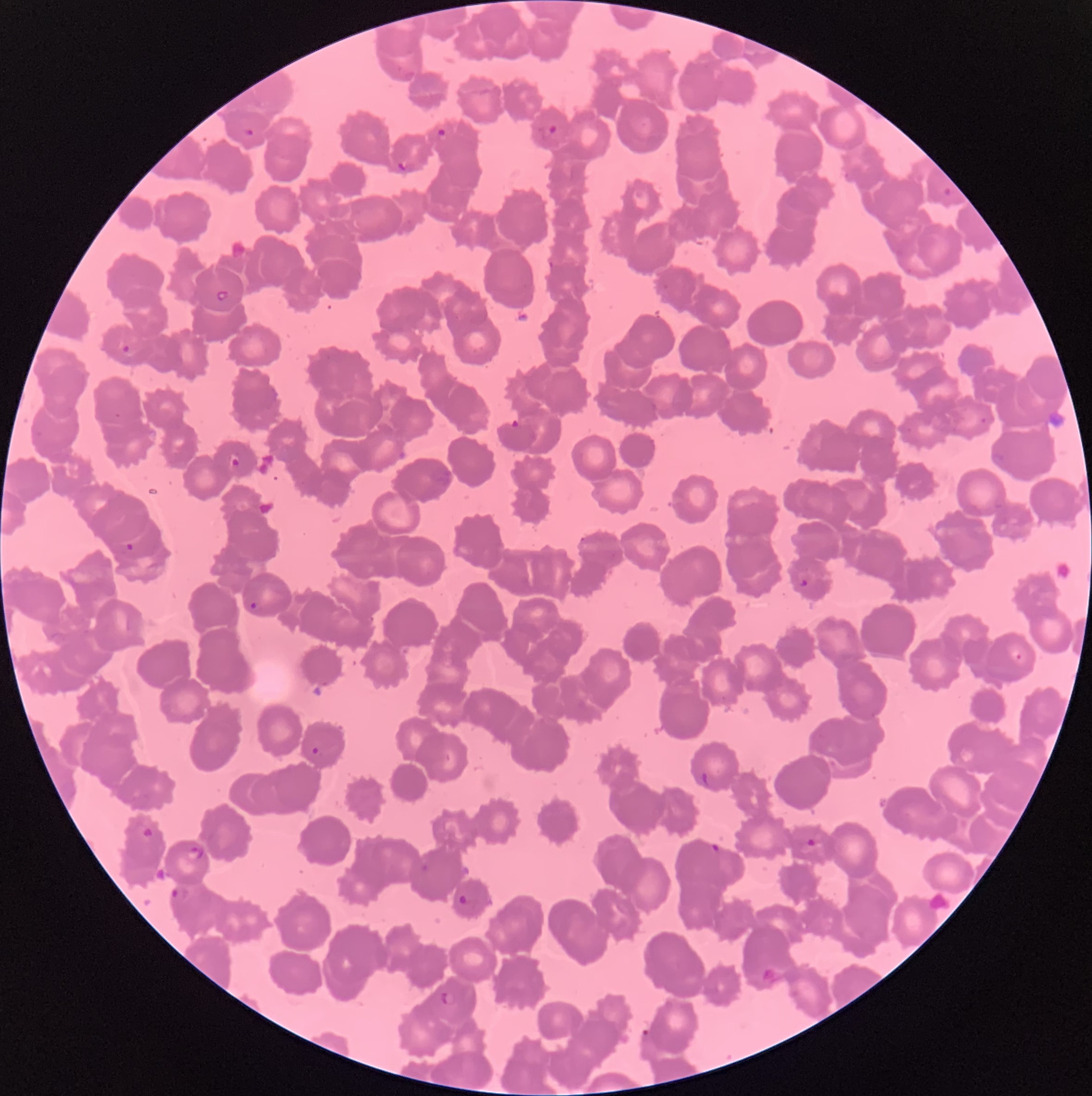

{
  "preparation": "thin blood smear",
  "image_size": "1092×1096 pixels",
  "modality": "optical microscopy",
  "plasmodium_parasite_locations": "approximate bounding boxes as named x1/y1/x2/y2 corners in pixels: (x1=540, y1=123, x2=557, y2=141), (x1=242, y1=125, x2=255, y2=138), (x1=434, y1=127, x2=449, y2=143), (x1=397, y1=160, x2=411, y2=173), (x1=942, y1=186, x2=953, y2=198), (x1=216, y1=289, x2=230, y2=302), (x1=121, y1=343, x2=131, y2=355), (x1=979, y1=416, x2=988, y2=425), (x1=227, y1=451, x2=241, y2=468), (x1=124, y1=541, x2=135, y2=552), (x1=798, y1=578, x2=809, y2=588), (x1=247, y1=600, x2=262, y2=612), (x1=1010, y1=649, x2=1024, y2=664), (x1=311, y1=745, x2=323, y2=760), (x1=140, y1=826, x2=156, y2=841), (x1=803, y1=837, x2=818, y2=850), (x1=710, y1=842, x2=723, y2=853), (x1=187, y1=845, x2=204, y2=860), (x1=169, y1=886, x2=189, y2=902), (x1=458, y1=894, x2=467, y2=905), (x1=440, y1=990, x2=457, y2=1008), (x1=641, y1=1027, x2=654, y2=1040)",
  "red_blood_cell_morphology": "rouleaux formation"
}